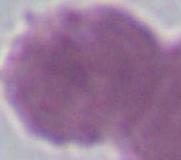

modality = photomicrograph
magnification = 1000x
identification = erythrocyte